Assess this cell for malaria.
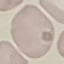
It is uninfected.

stain = Giemsa
image type = cell patch, automatically extracted from a larger field of view and resized to 64 × 64 pixels
capture = smartphone camera at the microscope eyepiece
preparation = thin blood smear